Comment on the morphology of the red blood cells.
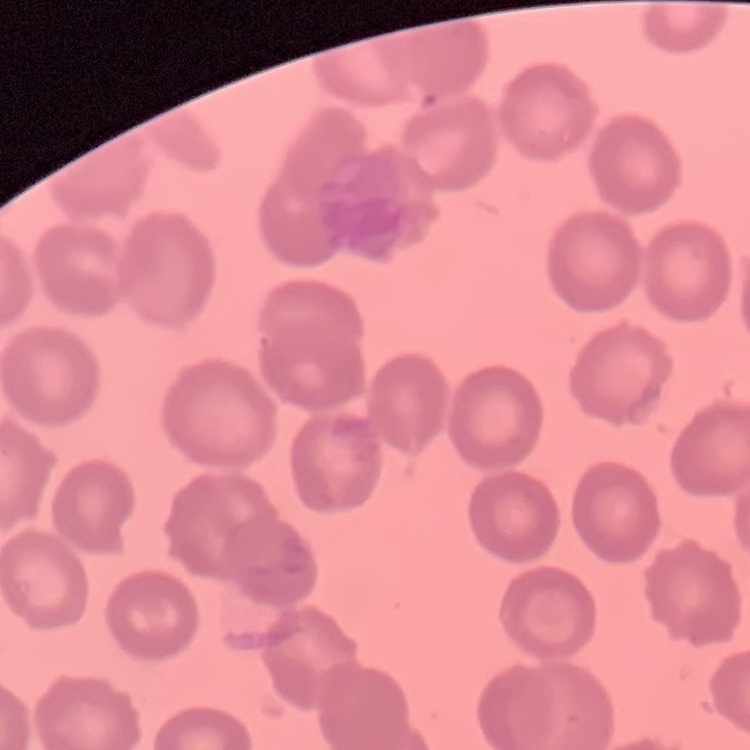
They show no rouleaux formation.

image type = one tile cut from a larger photomicrograph
preparation = thin blood smear
stain = Field's or Giemsa